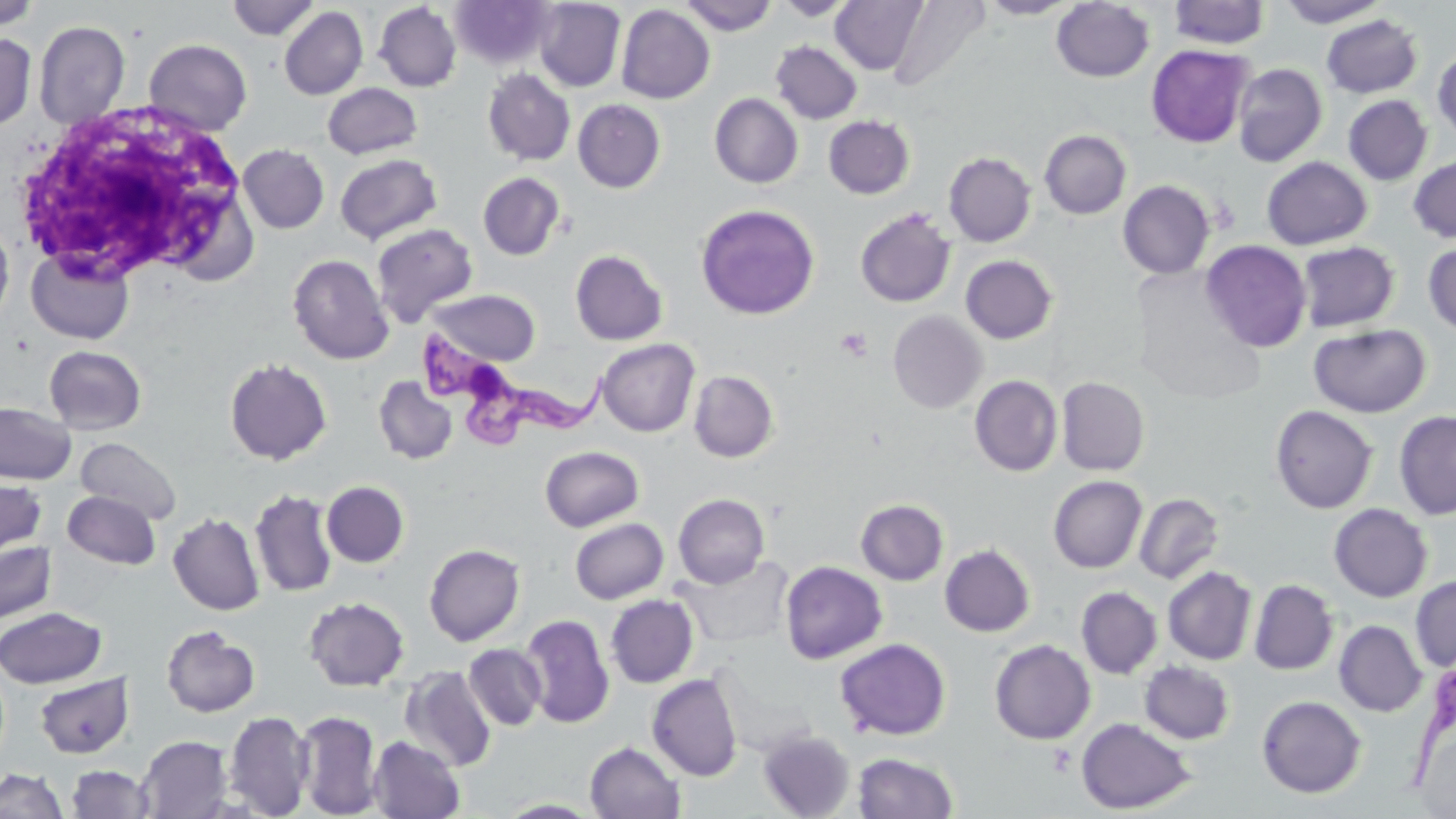
Summary:
  - Coordinate format: approximate bounding boxes as (x1, y1, x2, y2) in pixels
  - Trypanosoma brucei locations: (414, 329, 611, 451)
  - Uninfected red blood cell locations: (0, 0, 41, 32), (226, 0, 320, 40), (534, 0, 626, 92), (679, 0, 777, 35), (774, 0, 857, 20), (830, 0, 928, 75), (977, 0, 1080, 19), (1277, 0, 1388, 27), (450, 1, 553, 69), (888, 1, 991, 93), (1051, 1, 1155, 83), (1168, 1, 1271, 49), (373, 2, 461, 92), (616, 4, 715, 104), (279, 6, 368, 100), (1321, 14, 1423, 98), (33, 20, 130, 129), (0, 32, 37, 131), (143, 38, 252, 136), (770, 41, 862, 124), (1146, 44, 1253, 148), (1433, 49, 1456, 142), (1232, 63, 1327, 167), (482, 68, 576, 166), (322, 82, 422, 160), (710, 93, 803, 188), (1343, 95, 1432, 186), (573, 99, 666, 193), (823, 115, 915, 199), (1040, 130, 1131, 219), (238, 144, 330, 234), (944, 152, 1036, 247), (335, 153, 442, 244), (1408, 155, 1456, 243), (1261, 157, 1372, 249), (478, 172, 566, 260), (1118, 180, 1215, 279), (696, 204, 820, 319), (855, 208, 956, 307), (370, 222, 479, 327), (0, 223, 14, 328), (1201, 239, 1311, 352), (1296, 241, 1399, 332), (1423, 243, 1456, 336), (25, 247, 135, 345), (570, 250, 668, 345), (287, 253, 395, 365), (960, 255, 1057, 344), (426, 289, 542, 366), (888, 311, 986, 413), (1309, 323, 1431, 418), (597, 338, 700, 437), (44, 346, 147, 435), (224, 357, 332, 464), (689, 370, 779, 462), (373, 375, 458, 464), (970, 375, 1063, 476), (1056, 376, 1150, 476), (0, 401, 76, 485), (1269, 405, 1378, 514), (1394, 410, 1456, 520), (75, 437, 182, 525), (540, 445, 644, 532), (1048, 475, 1147, 573), (0, 477, 47, 557), (321, 481, 409, 567), (250, 488, 339, 598), (63, 490, 161, 570), (1134, 492, 1224, 585), (673, 493, 769, 588), (856, 499, 949, 585), (1329, 503, 1433, 602), (168, 511, 265, 616), (570, 518, 669, 604), (0, 541, 57, 625), (424, 543, 525, 646), (940, 544, 1035, 637), (675, 555, 797, 647), (779, 561, 887, 664), (1162, 566, 1257, 665), (1410, 575, 1456, 671), (1249, 579, 1338, 675), (1076, 587, 1162, 679), (605, 594, 698, 688), (303, 595, 410, 691), (0, 606, 107, 688), (520, 614, 614, 728), (1334, 620, 1427, 717), (161, 624, 260, 717), (835, 638, 951, 740), (989, 640, 1095, 745), (463, 643, 547, 731), (1139, 660, 1235, 744), (711, 661, 815, 758), (399, 667, 497, 773), (647, 673, 743, 781), (34, 674, 134, 759), (1256, 695, 1366, 798), (295, 709, 382, 817), (223, 710, 314, 817), (1075, 717, 1195, 815), (758, 729, 855, 818), (137, 736, 232, 818), (367, 736, 465, 819), (585, 741, 685, 819), (853, 752, 959, 818), (66, 765, 155, 818), (1, 768, 68, 818), (495, 799, 607, 818)
  - White blood cell locations: (9, 99, 257, 287)
  - Platelet locations: (835, 328, 873, 361)
  - Slide-level diagnosis: Trypanosoma brucei
  - Image size: 1456×819 pixels
  - Magnification: 1000x
  - Modality: light microscopy
  - Preparation: thin blood film
  - Stain: May-Grünwald-Giemsa
  - Field of view: single